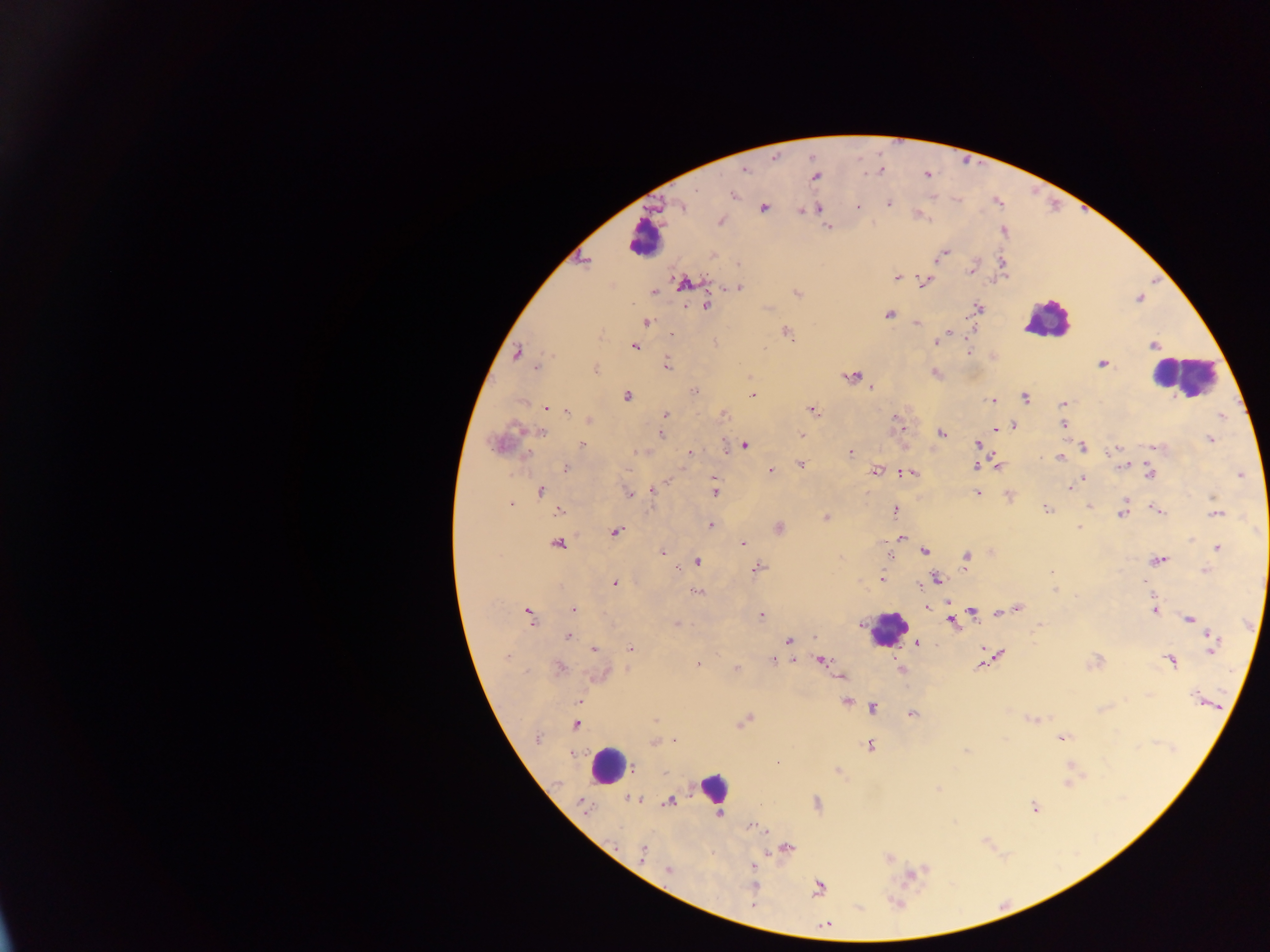
image_size: 1270×952 pixels
plasmodium_parasite_locations: 'approximate centers as (x, y) in pixels: (744, 170), (878, 170), (815, 177), (734, 195), (890, 204), (681, 207), (818, 208), (860, 208), (764, 210), (804, 210), (799, 211), (919, 215), (828, 226), (944, 251), (894, 277), (897, 278), (926, 282), (685, 283), (740, 288), (655, 292), (707, 305), (978, 306), (888, 313), (646, 321), (918, 322), (973, 329), (946, 334), (672, 336), (936, 342), (716, 343), (634, 346), (1152, 347), (971, 352), (516, 353), (667, 363), (1102, 363), (536, 367), (934, 373), (850, 377), (871, 387), (695, 392), (753, 392), (627, 396), (1025, 398), (991, 401), (1061, 404), (545, 407), (815, 412), (663, 415), (1062, 424), (1013, 426), (513, 428), (994, 430), (942, 433), (661, 435), (801, 435), (1210, 438), (977, 445), (582, 446), (744, 446), (1084, 446), (1120, 448), (638, 451), (1112, 451), (851, 452), (689, 453), (1058, 456), (801, 464), (997, 465), (1125, 465), (976, 466), (567, 467), (770, 469), (877, 471), (910, 472), (1243, 472), (903, 473), (1149, 473), (711, 478), (1084, 479), (714, 485), (1067, 488), (655, 490), (541, 491), (715, 493), (977, 493), (628, 494), (1007, 495), (1211, 497), (1125, 498), (512, 503), (1089, 506), (1046, 508), (1155, 509), (559, 510), (895, 510), (1162, 511), (1121, 514), (1215, 515), (825, 517), (710, 524), (1078, 527), (780, 528), (617, 532), (901, 537), (1191, 541), (559, 544), (742, 544), (1216, 548), (925, 550), (661, 551), (966, 557), (1154, 559), (889, 560), (1161, 560), (696, 561), (756, 567), (1204, 568), (1052, 572), (883, 578), (936, 578), (613, 582), (1054, 590), (696, 591), (927, 608), (1019, 608), (574, 609), (974, 612), (1154, 612), (528, 613), (761, 615), (998, 616), (530, 618), (1188, 620), (951, 622), (1210, 636), (567, 638), (573, 638), (788, 640), (916, 645), (628, 646), (593, 647), (981, 648), (1212, 650), (1001, 653), (507, 655), (772, 660), (1100, 660), (821, 661), (1170, 661), (698, 663), (979, 665), (735, 666), (561, 668), (590, 677), (839, 677), (1147, 695), (579, 700), (847, 700), (1122, 700), (873, 706), (913, 713), (655, 718), (1031, 719), (743, 722), (576, 724), (1060, 738), (674, 740), (1004, 740), (655, 743), (870, 744), (965, 750), (779, 763), (837, 770), (938, 788), (674, 797), (669, 801), (817, 802), (663, 804), (1035, 807), (719, 812), (757, 828), (763, 830), (786, 846), (642, 853), (886, 857), (750, 868), (669, 870), (908, 876), (818, 887), (751, 903)'
preparation: thick blood film
capture: mobile-phone photograph through a microscope
country: Ghana
field_of_view: single
leukocyte_locations: 'approximate centers as (x, y) in pixels: (648, 242), (1048, 327), (1170, 378), (887, 627), (608, 769), (714, 789)'